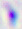
Summary:
  - Identification: Toxoplasma gondii
  - Modality: photomicrograph
  - Magnification: 400x